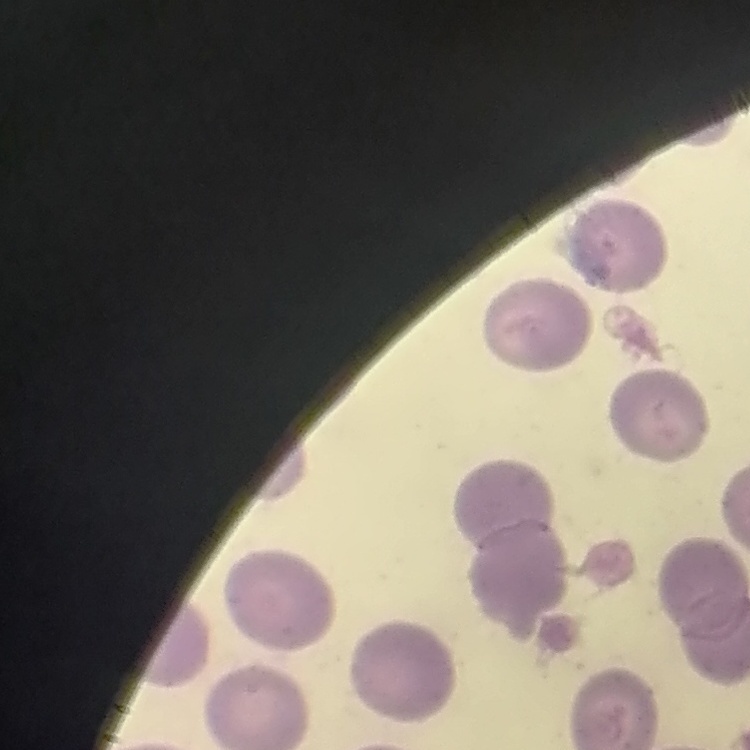

The erythrocytes show no rouleaux formation. Stained with either Field's or Giemsa. Square crop of a larger photomicrograph. Thin blood film.